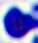
magnification = 400x
identification = white blood cell
modality = photomicrograph